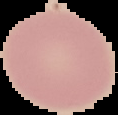
Summary:
  - Preparation: thin blood smear
  - Image type: cell region segmented out of the field of view; surrounding area masked to black
  - Image size: 118×115 pixels
  - Result: no Plasmodium parasites detected